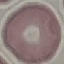
result = no malaria parasites seen
preparation = thin smear
image type = cell patch, automatically extracted from a larger field of view and resized to 64 × 64 pixels
stain = Giemsa
capture = smartphone camera at the microscope eyepiece